Give the extent of all Plasmodium vivax-infected red blood cells.
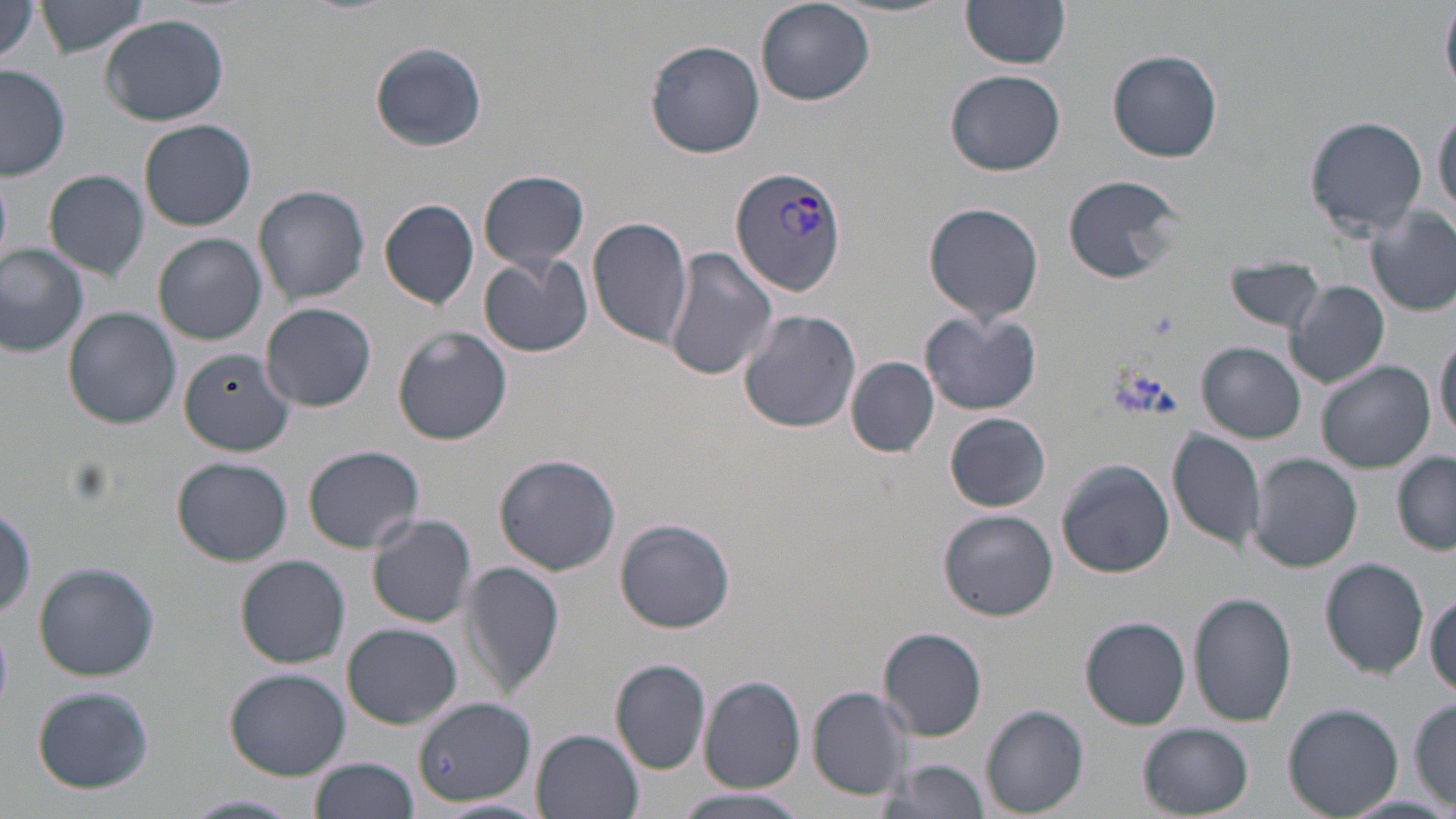

Approximate bounding boxes as (x1, y1, x2, y2) in pixels.
Plasmodium vivax-infected red blood cells: (731, 166, 846, 295).

Summary:
  - Uninfected red blood cell locations: (36, 0, 152, 58), (960, 0, 1073, 69), (0, 1, 45, 69), (755, 1, 875, 106), (1441, 4, 1455, 96), (101, 15, 228, 125), (644, 39, 765, 158), (370, 42, 486, 152), (1108, 49, 1223, 164), (0, 67, 72, 181), (947, 69, 1065, 176), (1433, 106, 1455, 218), (1306, 115, 1428, 235), (139, 118, 256, 231), (44, 170, 150, 283), (479, 170, 590, 272), (1062, 172, 1189, 285), (254, 184, 370, 306), (380, 198, 480, 309), (924, 201, 1046, 327), (1368, 207, 1456, 317), (588, 216, 693, 349), (153, 233, 266, 345), (0, 244, 89, 355), (663, 246, 776, 381), (479, 254, 591, 358), (1228, 258, 1328, 333), (1286, 281, 1389, 390), (261, 302, 377, 412), (738, 306, 862, 432), (63, 307, 182, 428), (920, 311, 1041, 416), (393, 327, 513, 445), (1435, 327, 1456, 447), (1198, 342, 1305, 442), (178, 347, 295, 455), (847, 358, 939, 457), (1317, 362, 1434, 474), (945, 411, 1050, 511), (1168, 429, 1267, 553), (303, 444, 423, 551), (1248, 453, 1362, 573), (493, 454, 621, 573), (1393, 454, 1455, 556), (171, 457, 293, 566), (1057, 459, 1174, 579), (938, 508, 1057, 621), (368, 514, 477, 627), (616, 519, 735, 633), (236, 555, 350, 668), (1320, 558, 1429, 678), (462, 560, 564, 697), (33, 561, 160, 682), (1427, 588, 1455, 699), (1188, 591, 1298, 727), (1080, 616, 1192, 730), (343, 623, 460, 728), (879, 627, 988, 740), (610, 660, 712, 774), (225, 668, 350, 780), (700, 675, 807, 793), (32, 685, 154, 795), (808, 686, 916, 800), (412, 696, 533, 806), (1411, 697, 1455, 810), (1284, 704, 1401, 818), (981, 705, 1088, 818), (1138, 722, 1253, 818), (532, 729, 643, 819), (310, 757, 420, 819), (883, 757, 991, 818), (675, 790, 808, 819), (183, 794, 304, 819)
  - Slide-level diagnosis: Plasmodium vivax
  - Modality: light microscopy
  - Preparation: thin blood smear
  - Stain: May-Grünwald-Giemsa
  - Image size: 1456×819 pixels
  - Field of view: single
  - Magnification: 1000x